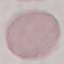

result = negative for malaria parasites
capture = smartphone through the microscope eyepiece
image type = cell patch, automatically extracted from a larger field of view and resized to 64 × 64 pixels
preparation = thin blood smear
stain = Giemsa